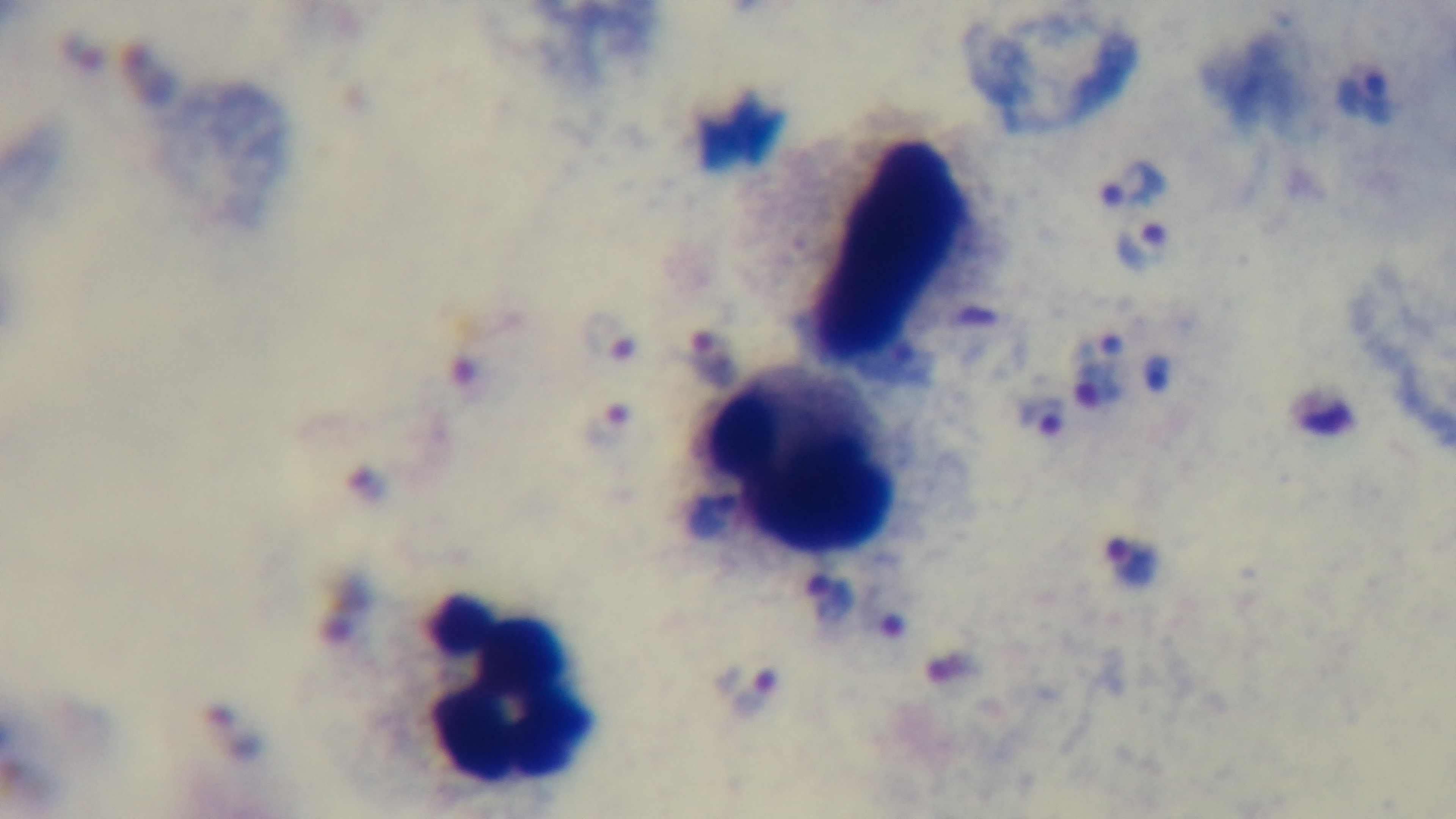

Preparation: thick smear. Giemsa stain. Single field of view. Light microscopy. Mounted 4K digital camera. 100x oil-immersion objective. Malaria status: positive.